Report the malaria status of this cell.
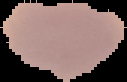

It is uninfected.

Summary:
  - Image size: 127×82 pixels
  - Preparation: thin blood film
  - Image type: cell region segmented out of the field of view; surrounding area masked to black